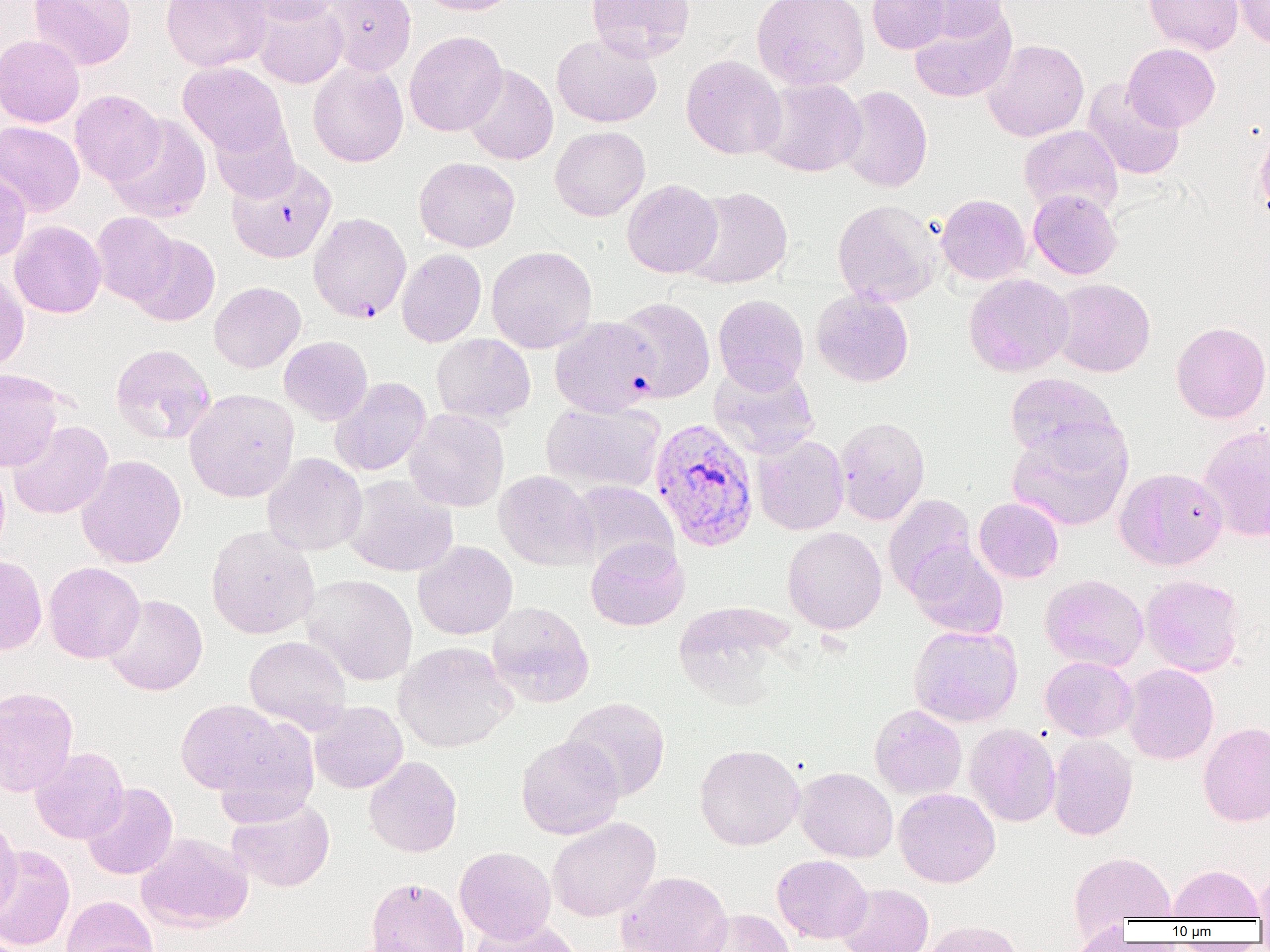
Plasmodium vivax-infected red blood cell locations = approximate bounding boxes as [x1, y1, x2, y2] in pixels: [308, 212, 412, 323], [550, 316, 660, 417], [649, 417, 759, 552]
slide-level diagnosis = Plasmodium vivax
modality = optical microscopy
field of view = single
uninfected red blood cell locations = approximate bounding boxes as [x1, y1, x2, y2] in pixels: [29, 0, 136, 70], [161, 0, 272, 72], [240, 0, 345, 24], [322, 0, 416, 75], [416, 0, 522, 15], [586, 0, 695, 62], [751, 0, 870, 91], [867, 0, 951, 54], [904, 0, 1012, 42], [1144, 0, 1243, 55], [1234, 0, 1270, 50], [251, 1, 348, 89], [909, 7, 1017, 103], [405, 31, 507, 137], [551, 32, 662, 128], [0, 34, 85, 127], [982, 39, 1089, 141], [1123, 43, 1220, 132], [681, 55, 786, 160], [307, 60, 408, 167], [178, 62, 289, 158], [463, 64, 559, 165], [757, 77, 866, 177], [1082, 79, 1185, 180], [836, 86, 932, 192], [70, 90, 164, 186], [106, 114, 212, 223], [210, 115, 300, 203], [0, 121, 84, 216], [1019, 125, 1123, 218], [550, 126, 650, 221], [414, 157, 520, 252], [227, 159, 337, 263], [0, 167, 31, 261], [622, 179, 722, 278], [683, 187, 793, 289], [1028, 190, 1122, 279], [935, 194, 1031, 285], [832, 200, 940, 307], [91, 212, 179, 305], [9, 221, 106, 318], [128, 234, 220, 327], [486, 246, 598, 353], [397, 248, 486, 347], [0, 271, 30, 374], [963, 273, 1074, 376], [1049, 278, 1156, 377], [209, 281, 306, 373], [811, 288, 914, 387], [713, 294, 809, 393], [611, 297, 715, 403], [1171, 321, 1270, 423], [431, 333, 536, 424], [279, 336, 373, 425], [110, 344, 216, 444], [709, 362, 819, 459], [0, 368, 64, 472], [1004, 373, 1122, 464], [330, 377, 431, 477], [184, 389, 300, 502], [541, 399, 666, 496], [404, 408, 509, 512], [834, 416, 930, 525], [8, 420, 113, 519], [1007, 422, 1133, 532], [1198, 424, 1270, 542], [752, 434, 849, 535], [262, 453, 368, 556], [76, 454, 187, 568], [0, 457, 10, 560], [1114, 467, 1228, 570], [494, 470, 599, 571], [343, 476, 457, 577], [567, 480, 679, 573], [883, 494, 978, 598], [973, 497, 1064, 583], [206, 524, 320, 639], [782, 526, 887, 635], [585, 537, 689, 631], [413, 540, 518, 640], [906, 542, 1008, 639], [0, 553, 47, 656], [44, 562, 145, 663], [301, 573, 418, 685], [1040, 573, 1148, 671], [1140, 574, 1245, 677], [102, 594, 207, 695], [486, 601, 595, 707], [671, 602, 795, 704], [908, 625, 1023, 727], [244, 635, 351, 731], [394, 642, 517, 753], [1040, 656, 1137, 741], [1122, 664, 1219, 765], [0, 686, 78, 797], [561, 697, 671, 801], [175, 698, 297, 799], [309, 701, 408, 793], [869, 704, 967, 800], [1198, 722, 1270, 827], [964, 723, 1060, 826], [1047, 734, 1138, 840], [516, 735, 625, 839], [694, 743, 804, 850], [30, 747, 129, 844], [364, 756, 462, 857], [794, 767, 897, 862], [81, 782, 178, 880], [894, 788, 1000, 888], [227, 797, 335, 892], [0, 815, 22, 922], [547, 817, 661, 921], [136, 832, 254, 932], [1, 845, 76, 950], [454, 846, 556, 945], [1069, 851, 1176, 927], [772, 854, 872, 944], [1166, 864, 1263, 921], [1254, 867, 1270, 921], [617, 870, 734, 952], [364, 876, 469, 952], [837, 883, 934, 952], [61, 895, 159, 952], [694, 908, 797, 952], [468, 919, 586, 952], [918, 920, 1025, 952], [1068, 921, 1132, 951]
preparation = thin blood film
magnification = 1000x
image size = 1270×952 pixels